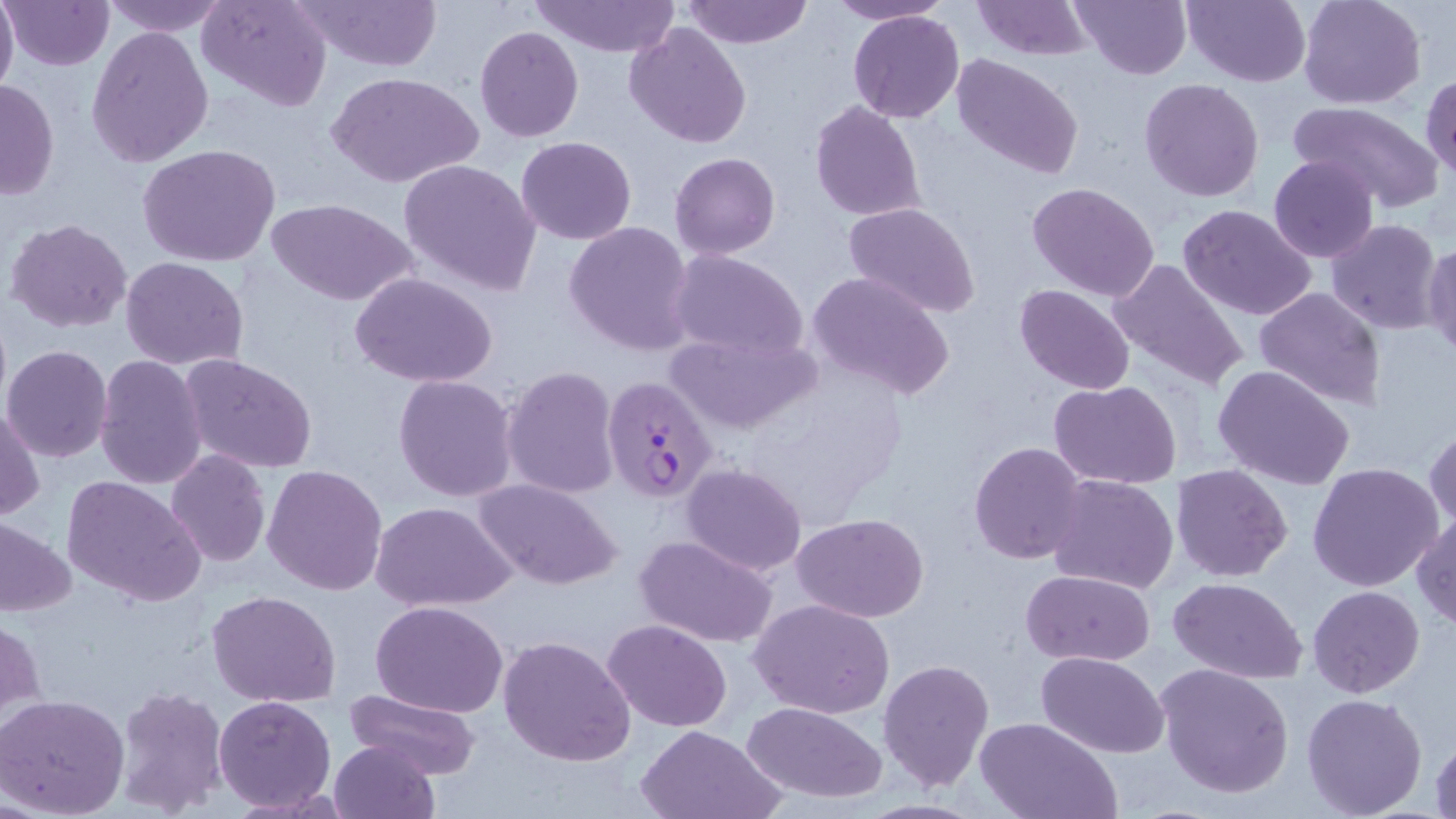
Summary:
  - Coordinate format: approximate bounding boxes as [x1, y1, x2, y2] in pixels
  - Plasmodium falciparum-infected red blood cell locations: [601, 374, 720, 504]
  - Uninfected red blood cell locations: [0, 0, 19, 98], [2, 0, 116, 71], [99, 0, 230, 37], [198, 0, 332, 112], [288, 0, 444, 73], [529, 0, 682, 57], [683, 0, 812, 48], [824, 0, 954, 25], [970, 0, 1093, 60], [1072, 0, 1191, 80], [1182, 0, 1312, 87], [1298, 0, 1426, 110], [847, 11, 965, 123], [624, 23, 752, 149], [475, 25, 584, 142], [86, 27, 215, 168], [950, 53, 1085, 180], [330, 72, 482, 189], [1421, 73, 1455, 183], [1, 78, 60, 202], [1139, 78, 1265, 203], [810, 101, 925, 222], [1288, 101, 1444, 210], [516, 136, 636, 244], [138, 143, 281, 267], [670, 152, 781, 259], [1268, 155, 1379, 263], [398, 158, 542, 297], [1028, 182, 1160, 303], [269, 199, 418, 307], [844, 202, 982, 318], [1177, 203, 1319, 319], [5, 217, 134, 335], [1326, 218, 1444, 336], [564, 221, 696, 355], [1422, 241, 1456, 360], [666, 249, 809, 363], [120, 257, 250, 370], [1107, 258, 1249, 393], [805, 270, 956, 401], [351, 273, 498, 388], [1014, 284, 1136, 393], [1254, 285, 1385, 409], [666, 329, 820, 435], [2, 345, 114, 464], [179, 353, 319, 475], [95, 356, 207, 489], [1212, 365, 1354, 490], [500, 366, 620, 501], [393, 374, 520, 503], [1050, 380, 1183, 488], [1, 403, 45, 521], [1425, 423, 1456, 533], [968, 442, 1088, 565], [165, 449, 271, 567], [1307, 462, 1445, 593], [261, 463, 387, 596], [680, 463, 807, 576], [1171, 464, 1293, 583], [1047, 474, 1179, 595], [61, 477, 206, 607], [473, 477, 624, 590], [370, 501, 517, 612], [792, 513, 929, 623], [1411, 514, 1456, 630], [0, 520, 75, 619], [634, 534, 778, 648], [1020, 569, 1154, 665], [1168, 575, 1308, 683], [1307, 585, 1426, 698], [207, 589, 342, 708], [751, 600, 895, 718], [371, 601, 510, 718], [1, 614, 45, 727], [603, 619, 731, 732], [498, 635, 636, 766], [1035, 652, 1170, 758], [878, 658, 994, 790], [1156, 664, 1293, 798], [112, 686, 229, 814], [343, 690, 480, 778], [1302, 692, 1429, 818], [0, 694, 130, 819], [214, 695, 337, 814], [742, 701, 887, 803], [975, 716, 1120, 819], [634, 725, 786, 819], [1429, 728, 1456, 819], [330, 738, 440, 819]
  - Slide-level diagnosis: Plasmodium falciparum
  - Preparation: thin blood film
  - Magnification: 1000x
  - Stain: May-Grünwald-Giemsa
  - Field of view: one of a larger specimen
  - Modality: optical microscopy
  - Image size: 1456×819 pixels